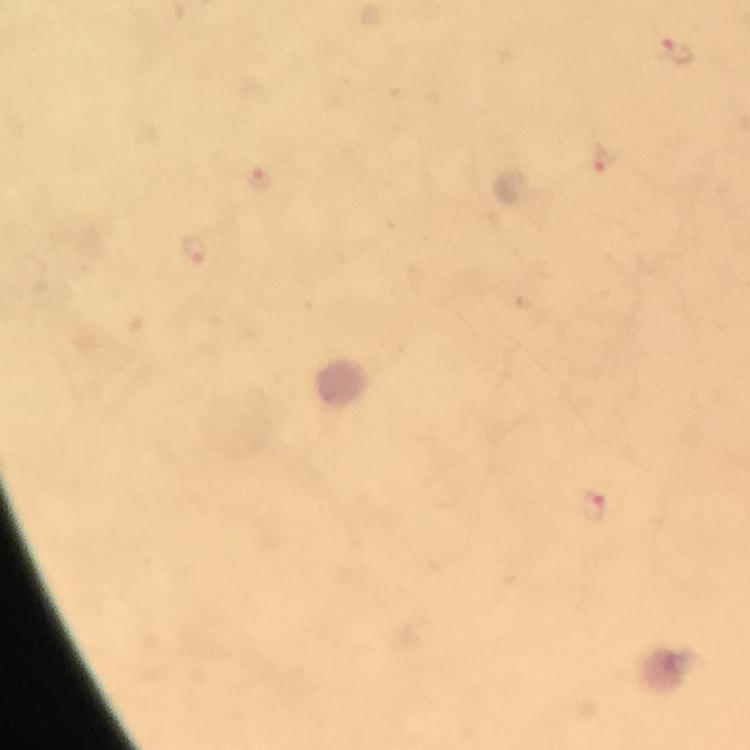
immersion oil = used
stain = Giemsa
image size = 750×750 pixels
capture = smartphone mounted on the microscope
malaria parasite locations = approximate centers as [x, y] in pixels: [674, 47], [603, 157], [593, 505]
context = from a diagnostic examination for malaria
preparation = thick smear
magnification = 100x
cropped from = a single field of view